Identify the blood parasite species.
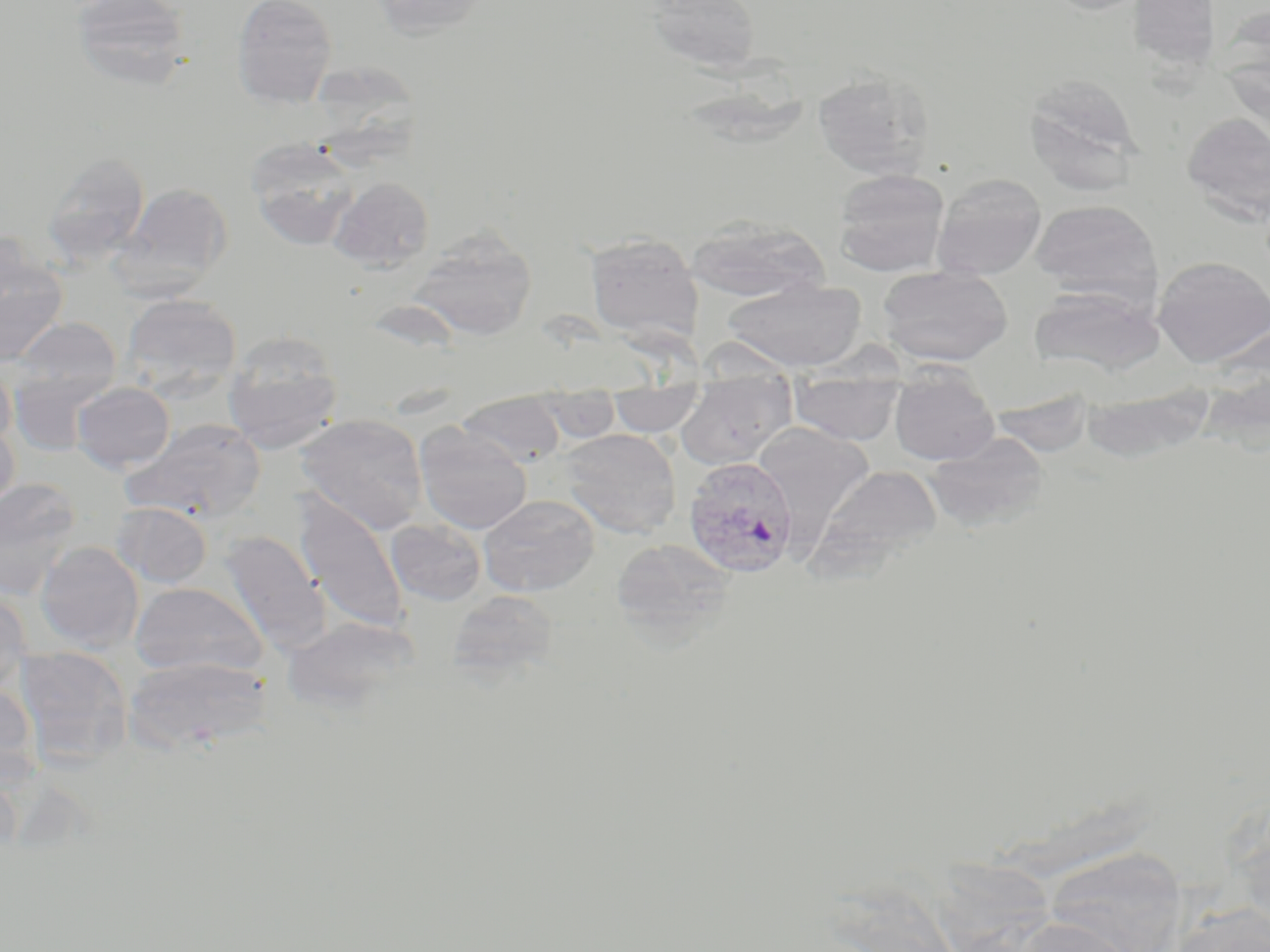

Plasmodium vivax.

{
  "uninfected_red_blood_cell_locations": "approximate bounding boxes as (x1,y1)-(x2,y2) corner pairs in pixels: (70,0)-(194,89), (232,0)-(338,109), (370,0)-(490,39), (646,0)-(762,73), (1041,0)-(1161,16), (1126,0)-(1221,73), (308,69)-(434,181), (811,69)-(934,180), (1023,74)-(1143,193), (1182,113)-(1270,223), (246,138)-(361,251), (42,151)-(150,267), (833,168)-(949,276), (931,173)-(1047,280), (329,176)-(435,272), (115,182)-(233,295), (1030,199)-(1161,303), (684,217)-(829,304), (406,228)-(537,341), (585,232)-(703,344), (0,243)-(68,366), (1153,255)-(1270,367), (877,265)-(1013,366), (723,279)-(866,371), (1030,284)-(1163,375), (120,293)-(242,398), (10,316)-(122,407), (223,332)-(343,453), (696,338)-(800,381), (0,360)-(16,451), (7,367)-(114,456), (890,374)-(999,466), (72,381)-(176,473), (789,383)-(903,444), (676,384)-(795,469), (1081,385)-(1216,466), (609,389)-(704,436), (454,394)-(566,467), (532,394)-(621,443), (295,414)-(428,535), (0,418)-(20,519), (122,419)-(266,523), (753,422)-(874,532), (413,423)-(533,534), (559,428)-(681,539), (923,431)-(1049,533), (811,464)-(944,571), (0,477)-(82,600), (292,493)-(411,636), (478,495)-(599,596), (112,502)-(212,588), (385,519)-(486,607), (218,530)-(329,655), (611,539)-(736,646), (36,542)-(144,652), (130,581)-(267,679), (0,589)-(32,697), (447,590)-(559,685), (283,616)-(419,714), (13,644)-(132,769), (124,656)-(273,754), (0,682)-(40,786), (1232,800)-(1270,935), (1045,848)-(1185,952), (1167,903)-(1270,952), (1006,916)-(1140,952)",
  "field_of_view": "one of a larger specimen",
  "image_size": "1270×952 pixels",
  "stain": "May-Grünwald-Giemsa",
  "modality": "optical microscopy",
  "preparation": "thin blood smear",
  "magnification": "1000x",
  "plasmodium_vivax_infected_red_blood_cell_locations": "approximate bounding boxes as (x1,y1)-(x2,y2) corner pairs in pixels: (683,456)-(799,577)"
}